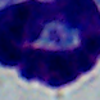
identification = white blood cell
magnification = 1000x
modality = micrograph